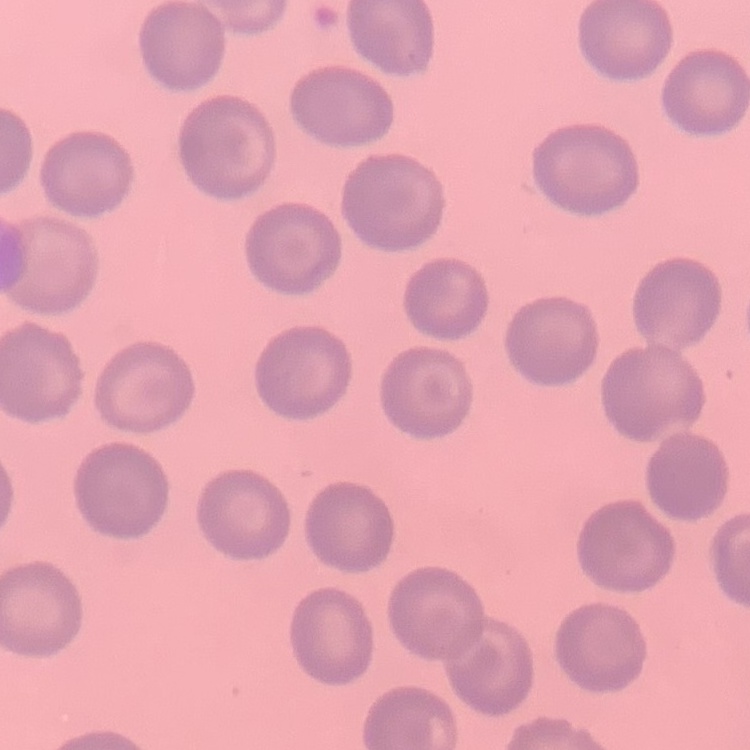

Summary:
  - Red blood cell morphology: no rouleaux formation
  - Stain: Field's or Giemsa
  - Image type: square crop of a larger photomicrograph
  - Preparation: thin blood film